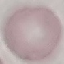
Malaria status: uninfected. Photographed with a smartphone camera at the microscope eyepiece. Cell patch, automatically extracted from a larger field of view and resized to 64 × 64 pixels. Giemsa-stained preparation. Thin blood film.